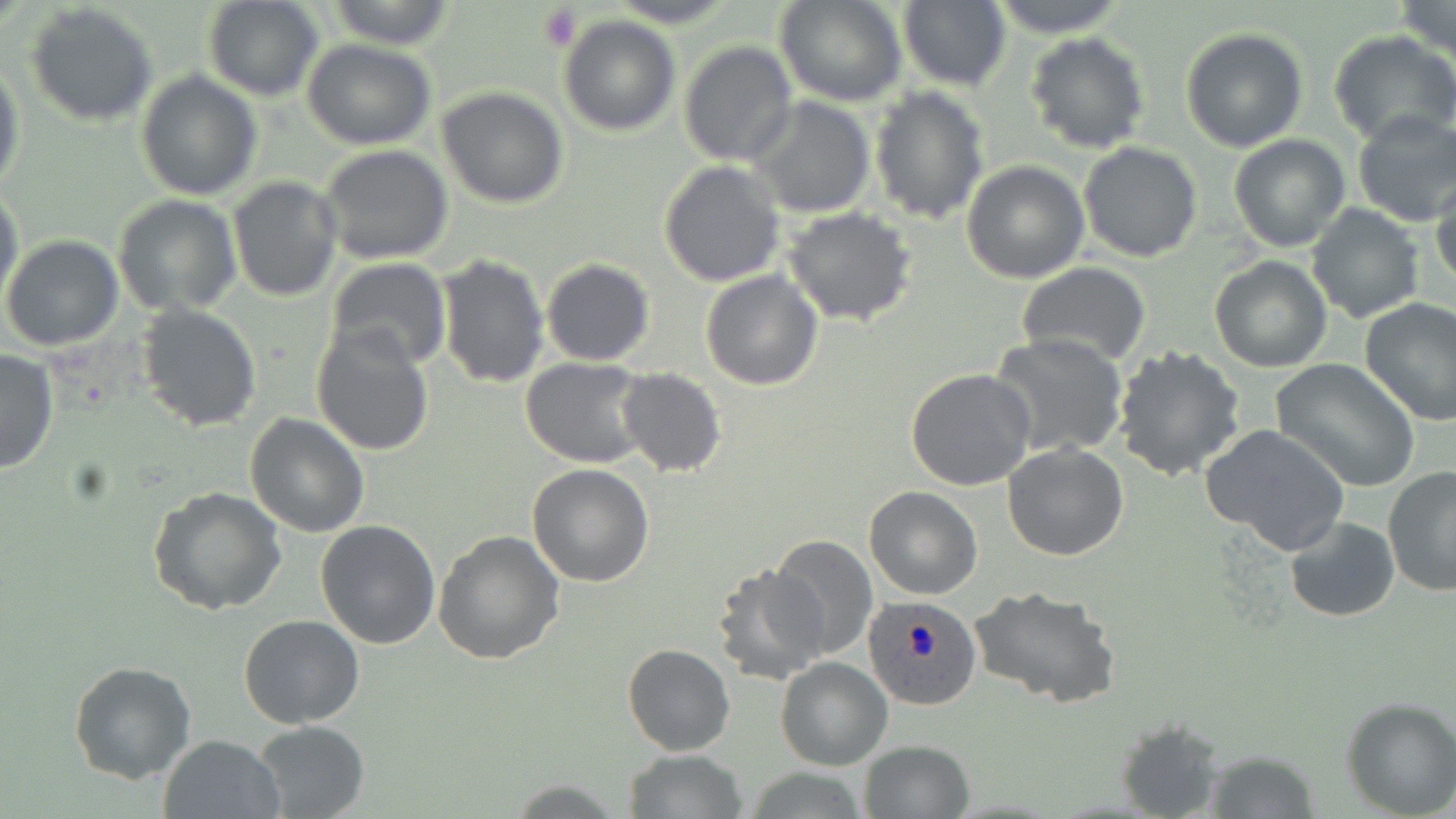
slide_level_diagnosis: Plasmodium ovale
image_size: 1456×819 pixels
platelet_locations: 'approximate bounding boxes as (x1,y1)-(x2,y2) corner pairs in pixels: (537,5)-(582,53)'
field_of_view: one of a larger specimen
uninfected_red_blood_cell_locations: 'approximate bounding boxes as (x1,y1)-(x2,y2) corner pairs in pixels: (609,0)-(739,27), (775,0)-(909,107), (984,0)-(1133,36), (203,1)-(324,101), (324,1)-(458,49), (898,1)-(1013,92), (1393,2)-(1455,59), (26,6)-(155,128), (557,15)-(681,135), (1180,27)-(1310,152), (1328,31)-(1456,148), (1022,32)-(1151,154), (301,39)-(438,149), (678,41)-(796,167), (0,60)-(24,199), (135,71)-(262,200), (869,85)-(990,225), (437,86)-(569,209), (745,95)-(877,219), (1350,110)-(1456,226), (1229,133)-(1351,252), (1078,140)-(1203,262), (319,145)-(453,265), (658,160)-(786,286), (961,160)-(1090,283), (1430,173)-(1456,291), (227,177)-(342,301), (0,185)-(23,310), (112,194)-(242,316), (1305,202)-(1426,323), (783,206)-(918,328), (2,234)-(123,351), (434,252)-(550,390), (1208,256)-(1332,372), (326,258)-(451,372), (541,259)-(653,365), (1018,262)-(1151,366), (699,270)-(823,391), (1358,297)-(1456,426), (137,304)-(263,432), (311,324)-(435,455), (988,333)-(1129,458), (1112,345)-(1245,482), (0,349)-(59,475), (521,357)-(653,468), (1272,358)-(1421,493), (616,368)-(727,478), (905,369)-(1037,492), (244,412)-(370,537), (1200,423)-(1351,557), (1002,444)-(1129,562), (527,464)-(656,587), (1382,466)-(1456,598), (864,486)-(982,600), (147,487)-(287,614), (1284,517)-(1400,621), (316,519)-(440,650), (433,530)-(565,665), (769,536)-(878,661), (711,564)-(831,686), (970,586)-(1119,708), (238,615)-(365,729), (622,644)-(735,756), (774,658)-(891,771), (67,661)-(196,784), (1341,697)-(1456,817), (1117,719)-(1228,818), (252,720)-(371,818), (157,733)-(286,819), (858,739)-(975,819), (626,748)-(746,818), (1202,748)-(1321,818), (743,767)-(872,818)'
stain: May-Grünwald-Giemsa
plasmodium_ovale_infected_red_blood_cell_locations: 'approximate bounding boxes as (x1,y1)-(x2,y2) corner pairs in pixels: (863,595)-(983,709)'
modality: light microscopy
preparation: thin blood smear
magnification: 1000x